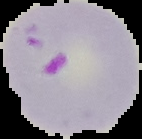

Cell region segmented out of the field of view; the surrounding area is masked to black. Image is 142×139 pixels. Malaria status: parasitized. From a thin blood smear.